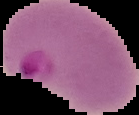
Cell region segmented out of the field of view; the surrounding area is masked to black. From a thin blood smear. Image is 139×115 pixels. Malaria status: parasitized.